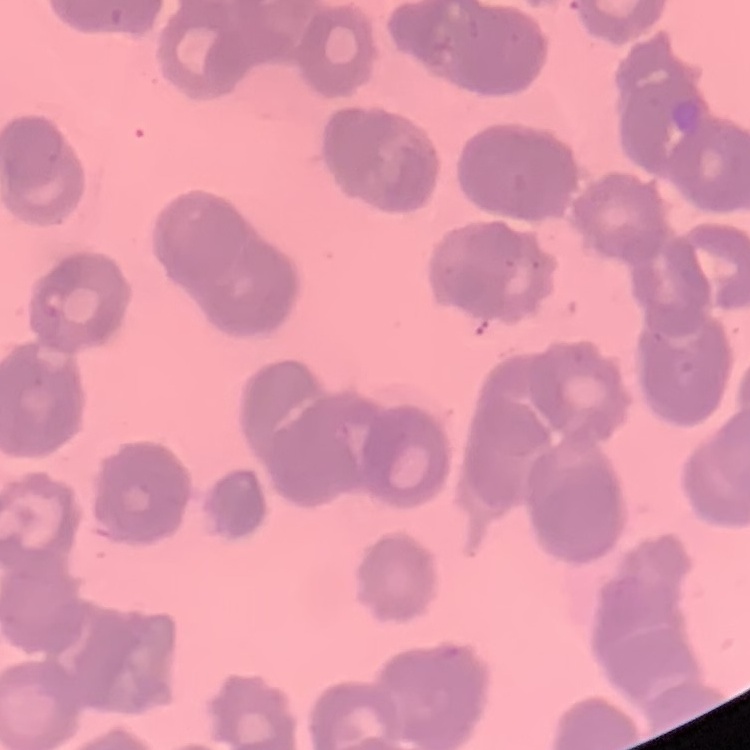

red blood cell morphology = rouleaux formation
preparation = thin blood smear
image type = square crop of a larger photomicrograph
stain = Field's or Giemsa